Identify the parasite.
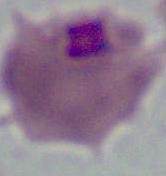

This is Plasmodium.

Captured at either 400x or 1000x magnification. Micrograph.